Report the malaria status of this cell.
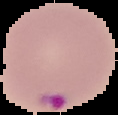
It is parasitized.

Summary:
  - Preparation: thin blood film
  - Image type: cell region segmented out of the field of view; surrounding area masked to black
  - Image size: 118×115 pixels